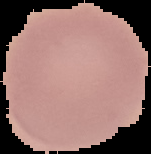

Malaria status: uninfected. Segmented cell region on a black background. From a thin blood film. Image is 151×154 pixels.